Comment on the morphology of the erythrocytes.
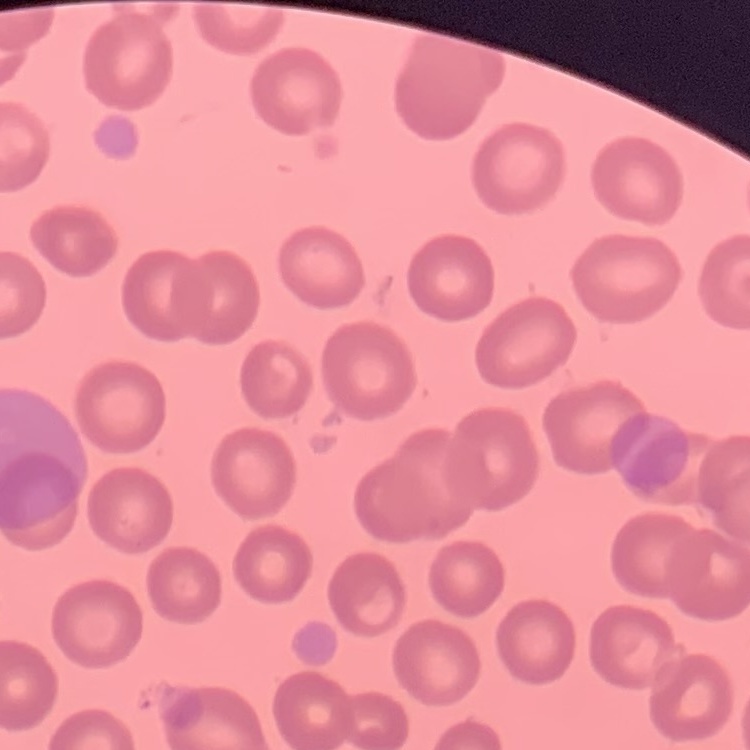

No rouleaux formation.

Thin blood smear. Square crop of a larger photomicrograph. Field's or Giemsa stain.